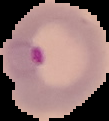
Summary:
  - Image type: segmented cell region with the area outside set to black
  - Preparation: thin blood film
  - Image size: 109×121 pixels
  - Result: Plasmodium parasites detected